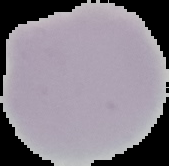
image size = 169×166 pixels
preparation = thin blood smear
malaria status = uninfected
image type = segmented cell region on a black background